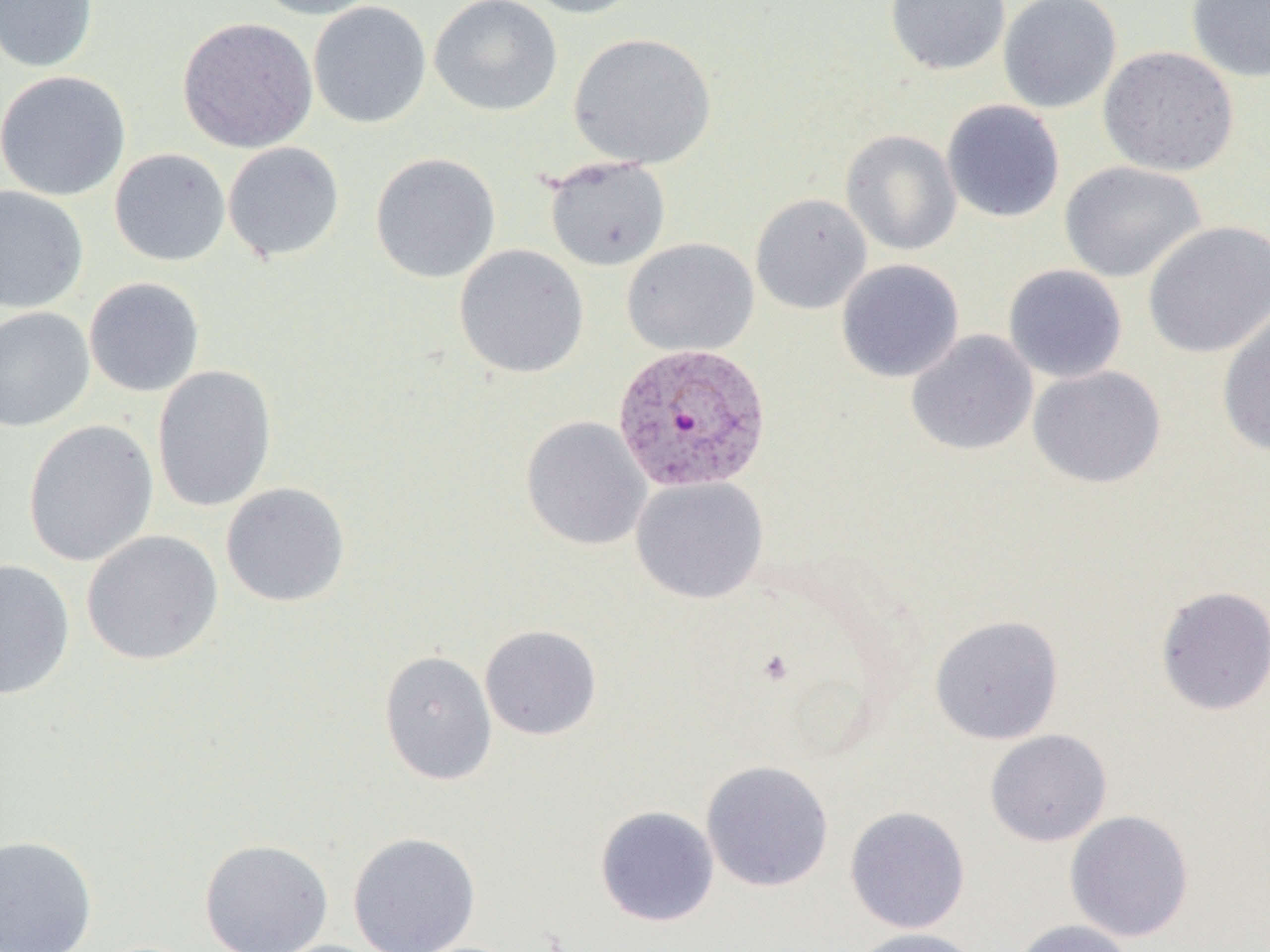

Approximate bounding boxes as (x1, y1, x2, y2) in pixels. Plasmodium vivax-infected red blood cell locations: (612, 340, 772, 492). Uninfected red blood cell locations: (0, 0, 99, 72), (250, 0, 388, 20), (429, 0, 563, 117), (519, 0, 646, 19), (885, 0, 1011, 75), (998, 0, 1122, 113), (1185, 0, 1270, 83), (309, 1, 431, 129), (177, 16, 318, 154), (568, 32, 717, 169), (1098, 45, 1240, 177), (0, 70, 131, 201), (941, 99, 1065, 223), (841, 129, 962, 256), (223, 141, 345, 262), (109, 148, 231, 267), (370, 152, 501, 283), (543, 156, 671, 271), (1059, 161, 1207, 283), (0, 184, 89, 313), (750, 193, 872, 314), (1142, 221, 1270, 359), (622, 238, 759, 356), (454, 244, 589, 379), (836, 259, 964, 383), (1003, 264, 1128, 383), (84, 277, 205, 397), (0, 306, 95, 432), (1216, 308, 1270, 458), (906, 329, 1038, 456), (152, 365, 277, 512), (1028, 365, 1167, 488), (521, 416, 652, 551), (23, 420, 159, 567), (630, 476, 768, 604), (221, 482, 351, 607), (81, 529, 223, 666), (0, 558, 75, 699), (1155, 585, 1270, 715), (929, 614, 1064, 745), (479, 624, 602, 741), (379, 650, 498, 786), (984, 729, 1112, 847), (700, 759, 834, 892), (594, 805, 720, 927), (844, 805, 971, 934), (1065, 810, 1195, 942), (348, 831, 481, 952), (0, 835, 98, 952), (199, 838, 334, 951), (1010, 919, 1137, 952), (848, 927, 985, 952). Slide-level diagnosis: Plasmodium vivax. Captured at 1000x magnification. Light microscopy. One field of a larger specimen. Thin blood film. Image is 1270×952 pixels.